Name the blood parasite species.
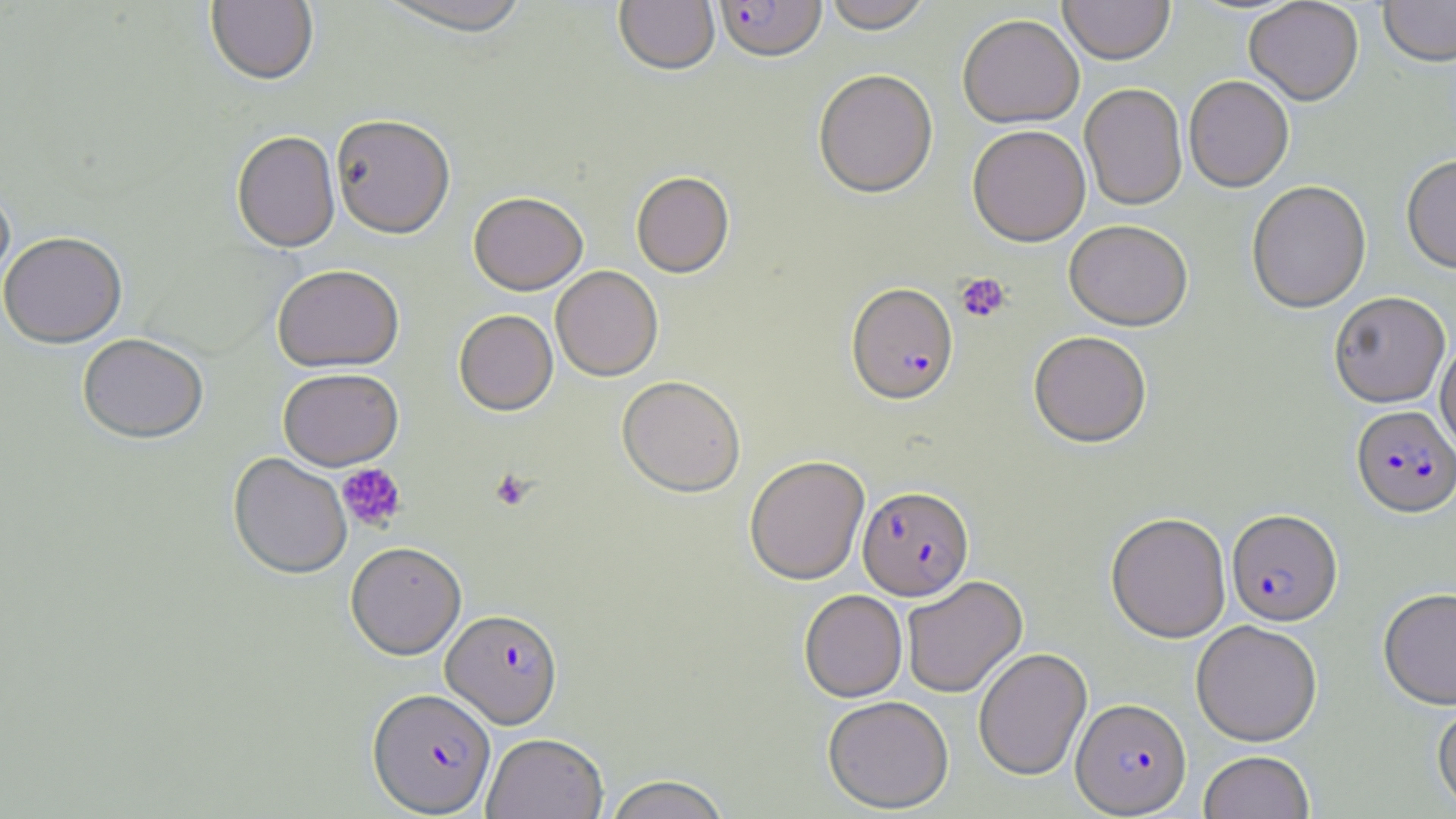
Plasmodium falciparum.

Summary:
  - Coordinate format: approximate bounding boxes as [x1, y1, x2, y2] in pixels
  - Uninfected red blood cell locations: [206, 0, 318, 85], [374, 0, 535, 38], [614, 0, 719, 77], [822, 0, 933, 35], [1059, 0, 1175, 66], [1379, 0, 1456, 70], [1244, 1, 1363, 107], [958, 16, 1084, 129], [813, 70, 938, 199], [1184, 77, 1294, 194], [1079, 84, 1187, 212], [330, 114, 455, 238], [968, 128, 1091, 248], [232, 130, 340, 251], [1401, 157, 1456, 276], [631, 172, 734, 278], [1247, 183, 1371, 315], [0, 184, 15, 295], [468, 192, 588, 295], [1064, 221, 1192, 332], [0, 230, 127, 348], [272, 264, 405, 371], [551, 266, 663, 381], [1329, 292, 1450, 408], [454, 310, 558, 415], [1029, 331, 1152, 448], [77, 332, 208, 442], [1436, 339, 1456, 459], [278, 367, 403, 470], [617, 376, 746, 497], [228, 452, 353, 579], [744, 456, 870, 585], [1106, 513, 1231, 643], [346, 541, 466, 659], [902, 576, 1028, 697], [1378, 589, 1456, 711], [799, 590, 908, 702], [1191, 621, 1322, 746], [973, 647, 1092, 781], [823, 696, 954, 813], [1432, 700, 1456, 815], [482, 732, 608, 819], [1198, 751, 1315, 819], [602, 774, 731, 818]
  - Platelet locations: [955, 273, 1011, 323], [337, 463, 407, 532], [489, 468, 536, 512]
  - Plasmodium falciparum-infected red blood cell locations: [715, 0, 827, 65], [846, 284, 958, 407], [1351, 406, 1456, 520], [858, 485, 975, 600], [1227, 510, 1343, 628], [442, 609, 563, 728], [367, 687, 496, 816], [1072, 698, 1191, 816]
  - Field of view: single
  - Magnification: 1000x
  - Stain: May-Grünwald-Giemsa
  - Modality: light microscopy
  - Preparation: thin blood smear
  - Image size: 1456×819 pixels